Report the malaria status of this cell.
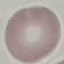

It is uninfected.

image type = automatically extracted cell patch, resized to 64 × 64 pixels
capture = smartphone through the microscope eyepiece
stain = Giemsa
preparation = thin smear